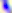

Captured at 400x magnification. Toxoplasma gondii is shown. Photomicrograph.